Identify the parasite.
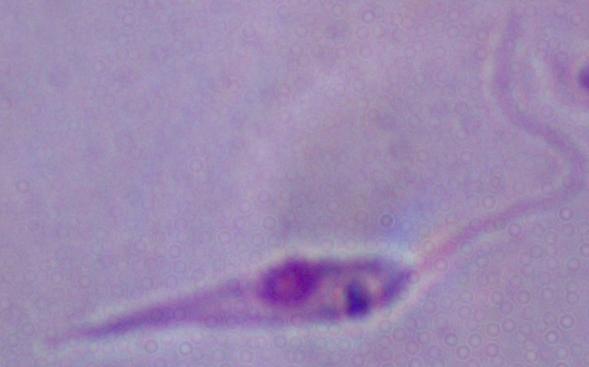

Leishmania.

1000x magnification. Photomicrograph.